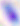

Summary:
  - Magnification: 400x
  - Identification: Toxoplasma gondii
  - Modality: photomicrograph